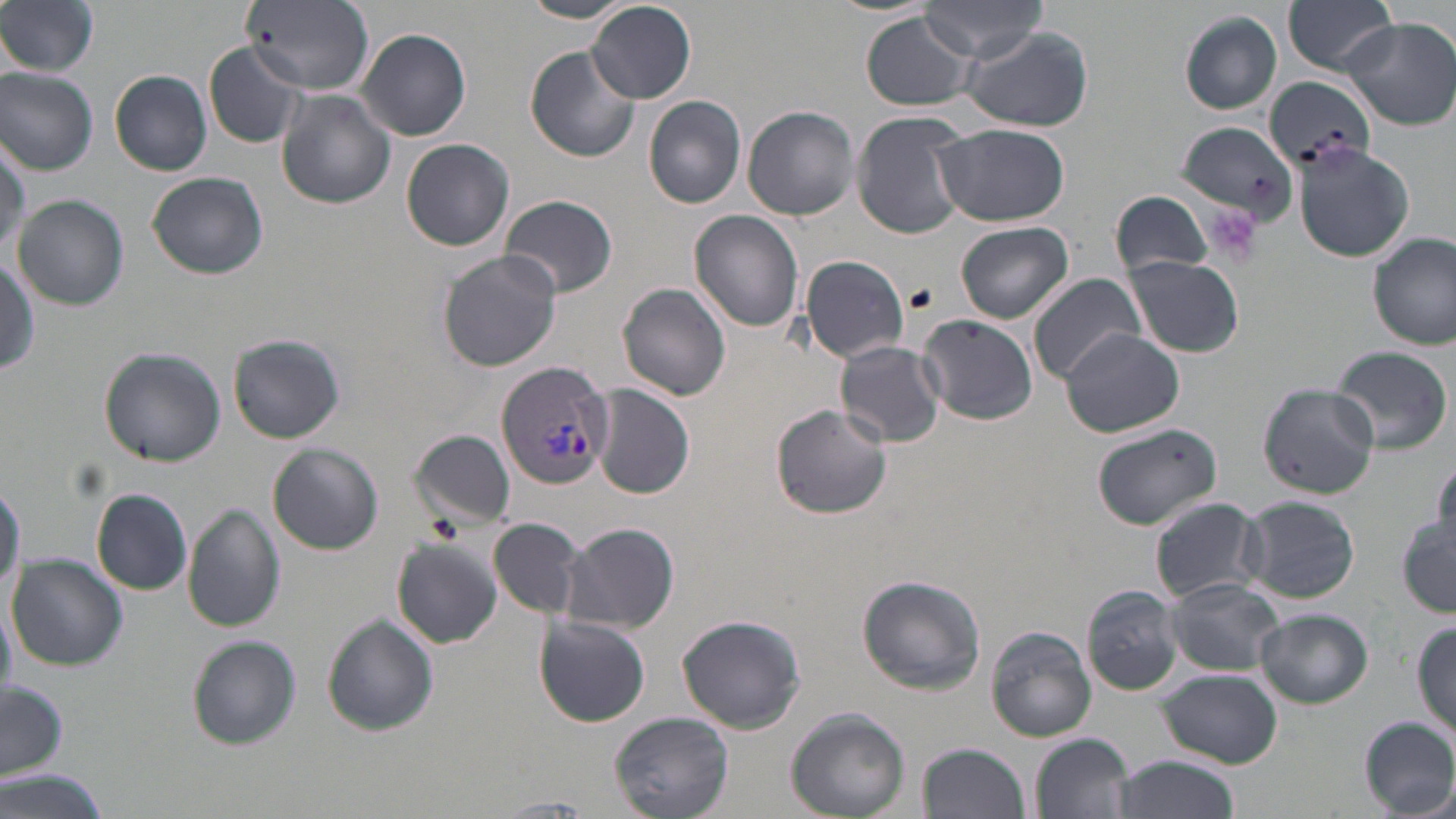

Approximate bounding boxes as (x1,y1)-(x2,y2) corner pairs in pixels. Platelet locations: (1204,205)-(1261,265). Plasmodium vivax-infected red blood cell locations: (497,361)-(617,490). Uninfected red blood cell locations: (0,0)-(100,77), (519,0)-(637,23), (921,0)-(1049,62), (1284,0)-(1398,75), (239,3)-(376,94), (589,3)-(697,102), (862,11)-(980,112), (1178,12)-(1282,114), (1340,16)-(1456,129), (958,25)-(1093,131), (357,29)-(471,141), (204,42)-(307,149), (526,46)-(640,163), (0,66)-(98,176), (110,69)-(212,176), (1263,76)-(1375,174), (277,90)-(397,209), (643,95)-(748,209), (743,105)-(860,220), (852,112)-(971,239), (1177,121)-(1300,228), (934,124)-(1069,228), (0,138)-(27,258), (401,138)-(515,251), (1292,141)-(1416,263), (148,172)-(269,280), (1112,190)-(1214,281), (11,194)-(128,310), (499,195)-(617,299), (689,210)-(805,331), (956,221)-(1075,324), (1369,234)-(1455,350), (438,250)-(562,372), (0,254)-(41,378), (799,254)-(911,362), (1126,257)-(1244,358), (1029,272)-(1145,383), (617,282)-(733,400), (916,314)-(1037,425), (1060,327)-(1185,438), (228,333)-(346,444), (836,341)-(947,447), (1329,344)-(1452,456), (98,348)-(225,466), (1256,380)-(1382,499), (591,385)-(698,499), (771,403)-(892,519), (1091,422)-(1224,531), (412,430)-(516,529), (268,443)-(383,554), (1430,458)-(1455,554), (0,475)-(22,611), (92,488)-(191,595), (1238,496)-(1360,604), (1150,498)-(1263,603), (184,504)-(285,632), (488,516)-(588,619), (1398,516)-(1455,617), (561,521)-(679,634), (391,538)-(503,648), (8,553)-(127,671), (855,574)-(986,694), (1165,578)-(1284,675), (1082,586)-(1183,696), (1254,608)-(1374,708), (676,614)-(807,734), (321,616)-(439,735), (533,616)-(651,727), (1412,620)-(1456,736), (987,626)-(1097,742), (187,635)-(300,748), (1159,671)-(1281,766), (0,681)-(69,779), (788,708)-(910,818), (611,710)-(734,818), (1359,716)-(1456,816), (1031,733)-(1135,819), (918,742)-(1031,819), (1108,755)-(1241,819), (1,772)-(111,818), (487,796)-(601,815). Slide-level diagnosis: Plasmodium vivax. Single field of view. Thin blood smear. May-Grünwald-Giemsa-stained preparation. Captured at 1000x magnification. Image is 1456×819 pixels. Optical microscopy.